Locate every malaria parasite.
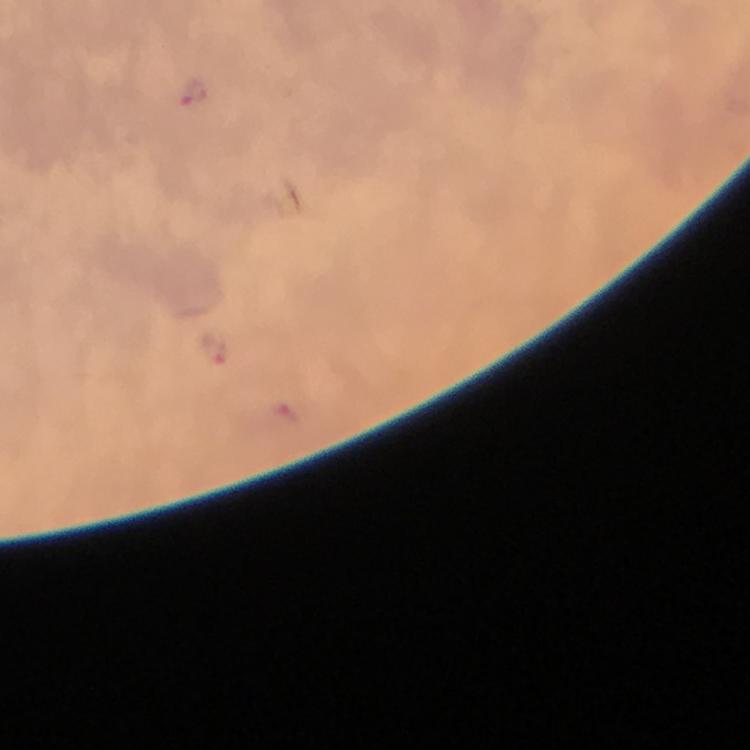
Approximate object centers, in pixels from the top-left corner.
Malaria parasites: (x=193, y=92), (x=213, y=351).

Summary:
  - Magnification: 100x
  - Capture: smartphone mounted on the microscope
  - Image size: 750×750 pixels
  - Preparation: thick blood film
  - Stain: Giemsa
  - Immersion oil: applied
  - Context: from a diagnostic examination for malaria
  - Cropped from: a single field of view